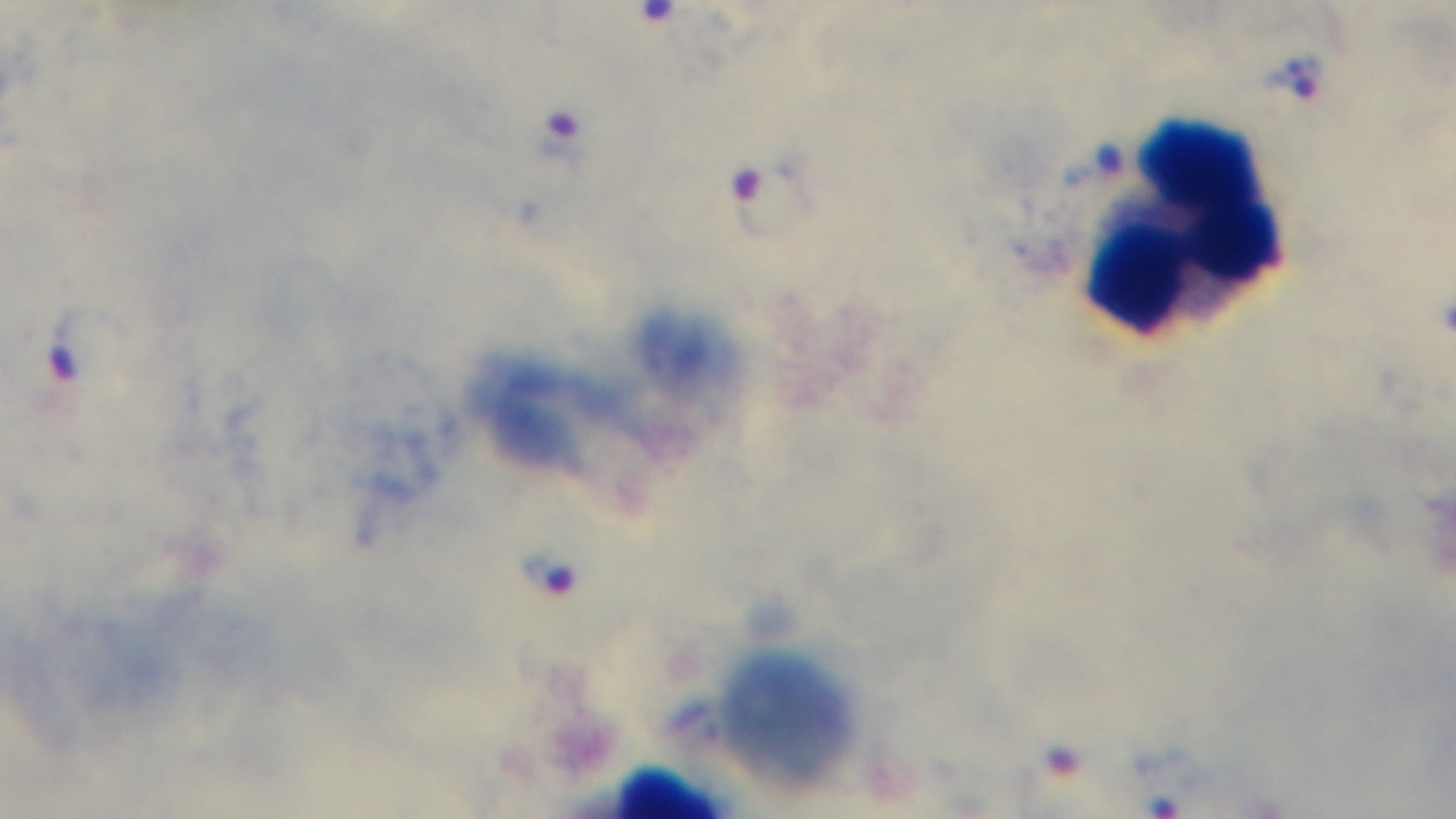
capture = mounted 4K digital camera
preparation = thick blood film
modality = light microscopy
field of view = one from the slide
objective = 100x oil immersion
stain = Giemsa
malaria status = infected